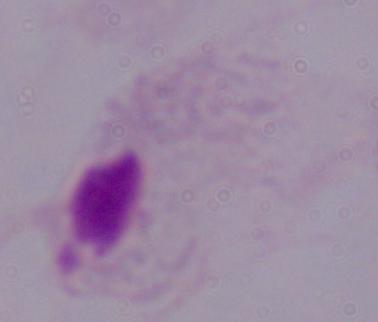

modality: micrograph
magnification: 1000x
identification: trichomonad